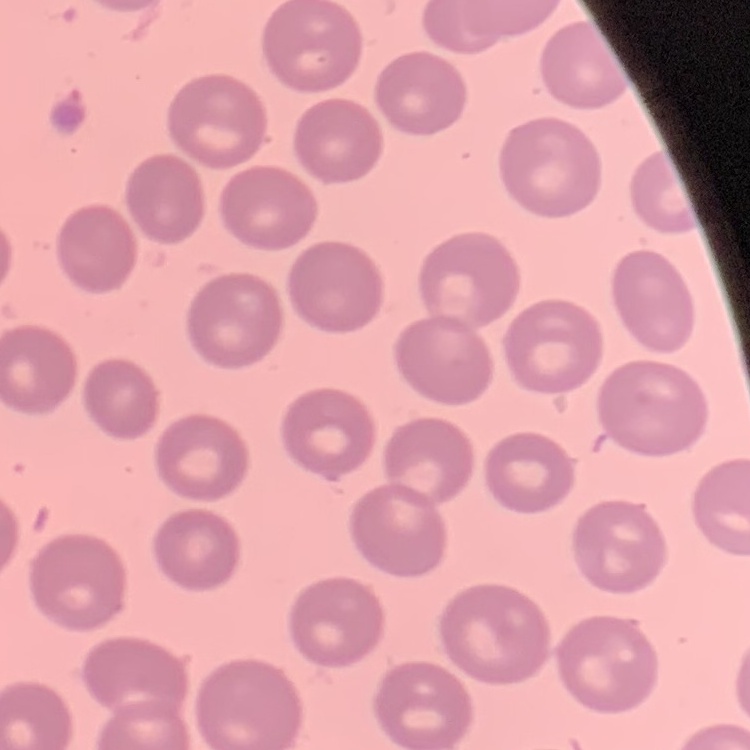

Summary:
  - Erythrocyte morphology: no rouleaux formation
  - Image type: square crop of a larger photomicrograph
  - Preparation: thin blood film
  - Stain: Field's or Giemsa